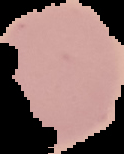
Image is 124×154 pixels. From a thin blood film. Malaria status: uninfected. Segmented cell region on a black background.